Comment on the morphology of the erythrocytes.
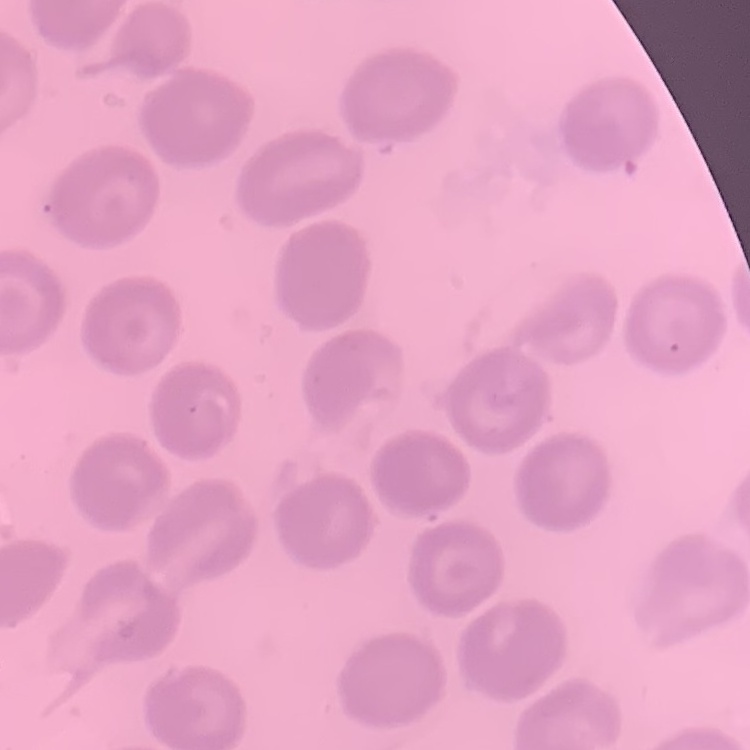

They show no rouleaux formation.

image type = one tile cut from a larger photomicrograph
preparation = thin blood smear
stain = Field's or Giemsa